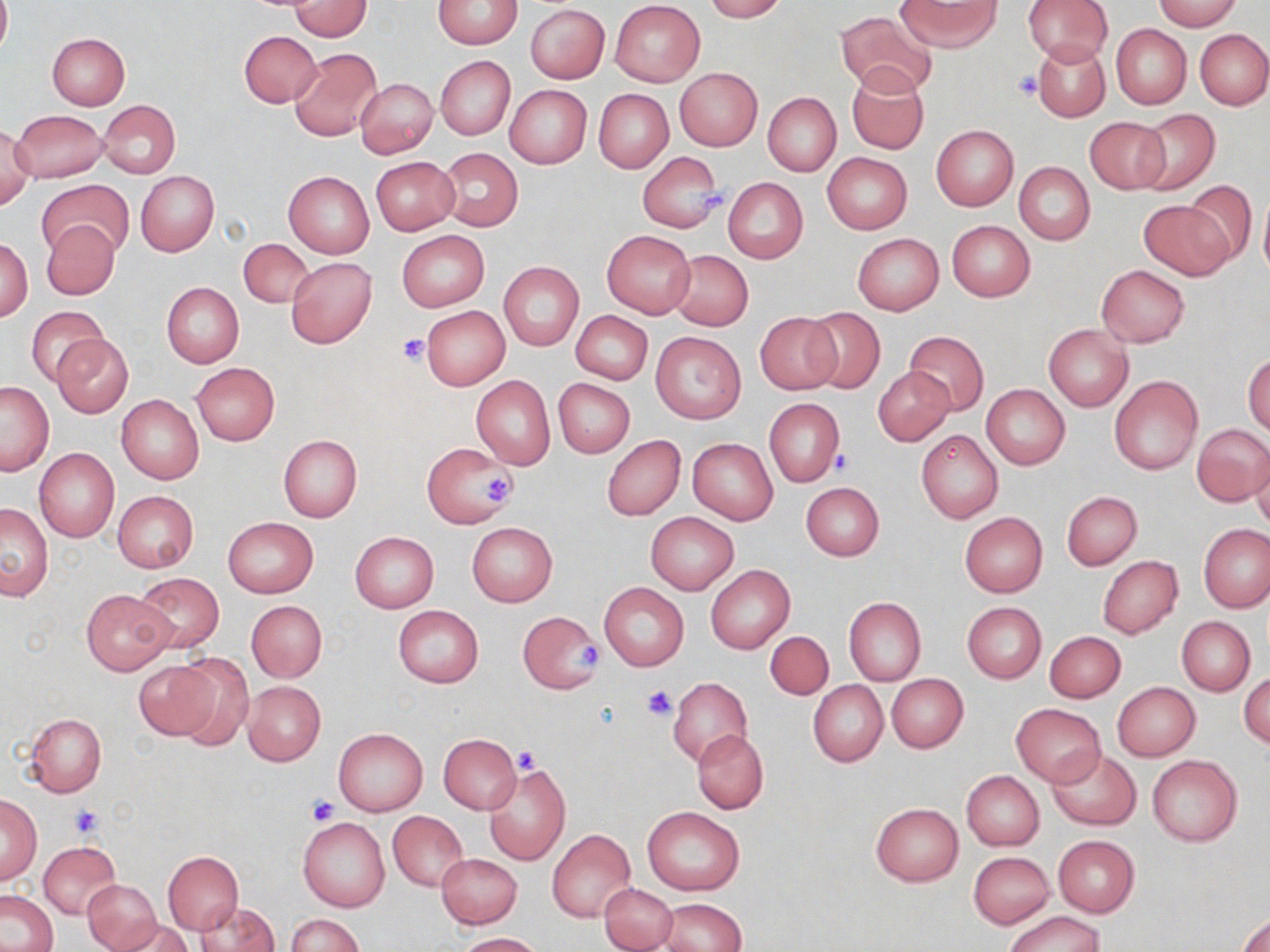

Approximate bounding boxes as [x1, y1, x2, y2] in pixels. Platelet locations: [1013, 70, 1043, 100], [689, 179, 738, 213], [396, 332, 433, 366], [830, 448, 858, 477], [479, 475, 516, 505], [570, 640, 600, 671], [641, 683, 678, 720], [512, 744, 544, 776], [308, 796, 338, 825], [70, 805, 103, 838]. Uninfected red blood cell locations: [0, 0, 11, 57], [703, 0, 786, 21], [896, 0, 1002, 50], [1023, 0, 1113, 65], [1151, 0, 1241, 30], [288, 1, 370, 40], [433, 1, 523, 48], [611, 1, 705, 86], [526, 5, 609, 83], [834, 10, 938, 96], [1111, 24, 1191, 108], [1196, 29, 1270, 109], [240, 30, 323, 107], [47, 32, 130, 110], [1034, 40, 1110, 123], [290, 48, 383, 140], [436, 56, 516, 141], [846, 67, 931, 156], [675, 68, 762, 151], [356, 78, 438, 159], [504, 85, 591, 168], [593, 88, 674, 174], [763, 91, 841, 175], [98, 100, 181, 178], [1131, 108, 1220, 196], [12, 110, 107, 183], [1085, 116, 1171, 193], [1, 125, 34, 214], [930, 125, 1019, 210], [438, 149, 522, 231], [638, 151, 723, 233], [822, 152, 913, 234], [371, 156, 460, 234], [1014, 162, 1095, 245], [136, 171, 219, 256], [284, 171, 374, 258], [724, 178, 807, 263], [38, 179, 134, 260], [1184, 180, 1257, 266], [1259, 189, 1270, 284], [1139, 199, 1235, 281], [41, 220, 119, 300], [946, 220, 1035, 301], [602, 230, 696, 319], [398, 231, 488, 311], [852, 233, 944, 315], [238, 237, 313, 309], [1, 238, 33, 321], [667, 250, 753, 329], [286, 256, 377, 348], [498, 261, 583, 350], [1096, 265, 1189, 347], [161, 282, 243, 367], [27, 306, 109, 386], [421, 306, 509, 390], [801, 307, 885, 393], [570, 311, 652, 384], [755, 312, 842, 394], [1043, 325, 1134, 411], [651, 331, 746, 423], [905, 331, 988, 414], [49, 333, 134, 419], [1244, 352, 1270, 435], [190, 362, 280, 445], [873, 368, 955, 444], [471, 374, 555, 469], [1109, 375, 1203, 474], [553, 377, 635, 458], [1, 381, 54, 475], [982, 384, 1070, 470], [116, 395, 204, 484], [764, 399, 844, 486], [1192, 423, 1270, 506], [916, 429, 1003, 524], [278, 434, 362, 523], [602, 435, 684, 519], [688, 437, 778, 525], [423, 441, 515, 530], [1250, 441, 1270, 530], [35, 449, 119, 541], [800, 482, 885, 560], [112, 491, 199, 573], [1061, 491, 1141, 570], [1, 503, 53, 599], [646, 512, 738, 594], [960, 512, 1047, 597], [223, 517, 318, 597], [466, 522, 558, 607], [1200, 524, 1270, 612], [350, 532, 439, 611], [1096, 555, 1183, 640], [705, 565, 795, 653], [134, 573, 223, 653], [599, 582, 689, 670], [82, 589, 177, 674], [843, 597, 925, 686], [247, 600, 327, 682], [961, 602, 1046, 682], [393, 605, 483, 687], [517, 611, 602, 693], [1177, 616, 1255, 696], [765, 631, 833, 699], [1045, 631, 1125, 702], [167, 655, 254, 747], [134, 658, 224, 740], [1239, 670, 1269, 749], [886, 673, 968, 753], [668, 677, 752, 767], [242, 680, 325, 766], [808, 680, 888, 767], [1112, 682, 1200, 761], [1011, 704, 1106, 787], [26, 714, 106, 796], [334, 728, 427, 817], [692, 729, 769, 813], [439, 734, 520, 813], [1048, 749, 1140, 830], [1147, 754, 1243, 847], [481, 759, 571, 866], [962, 771, 1044, 851], [0, 796, 40, 882], [870, 803, 964, 886], [642, 806, 744, 896], [388, 811, 469, 890], [298, 816, 390, 912], [547, 829, 635, 922], [1053, 835, 1139, 916], [39, 841, 122, 920], [969, 851, 1055, 928], [163, 852, 243, 934], [437, 853, 521, 929], [82, 880, 161, 951], [600, 884, 677, 950], [1, 890, 57, 951], [656, 899, 747, 952], [196, 900, 279, 952], [1003, 911, 1107, 952], [1237, 912, 1270, 952], [287, 914, 363, 951], [112, 917, 193, 952], [457, 932, 544, 951]. Slide-level diagnosis: no evidence of blood parasites. Image is 1270×952 pixels. Thin blood film. May-Grünwald-Giemsa stain. One field of a larger specimen. Optical microscopy. 1000x magnification.